Assess the morphology of the erythrocytes.
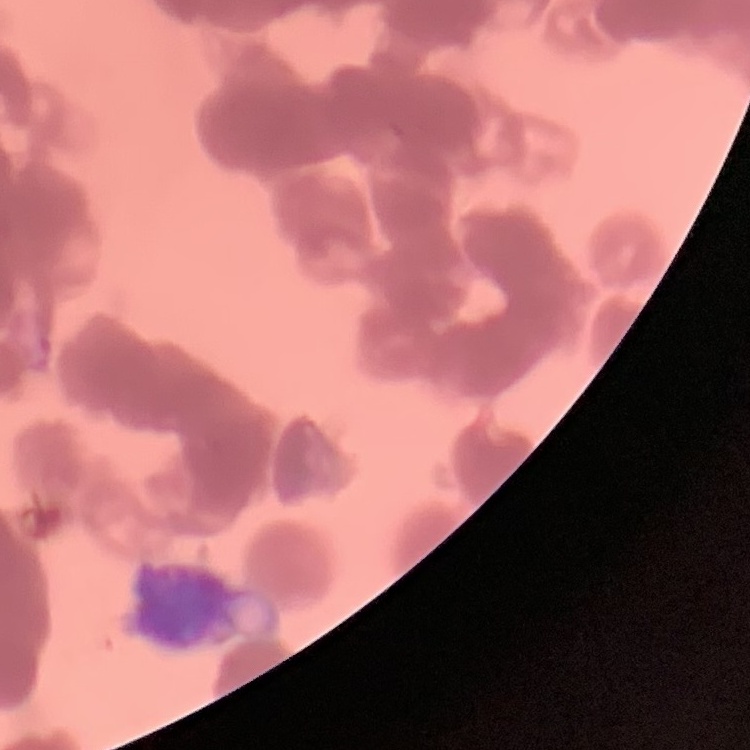

They show rouleaux formation.

Summary:
  - Stain: Field's or Giemsa
  - Image type: one tile cut from a larger photomicrograph
  - Preparation: thin blood film